Outline every leukocyte.
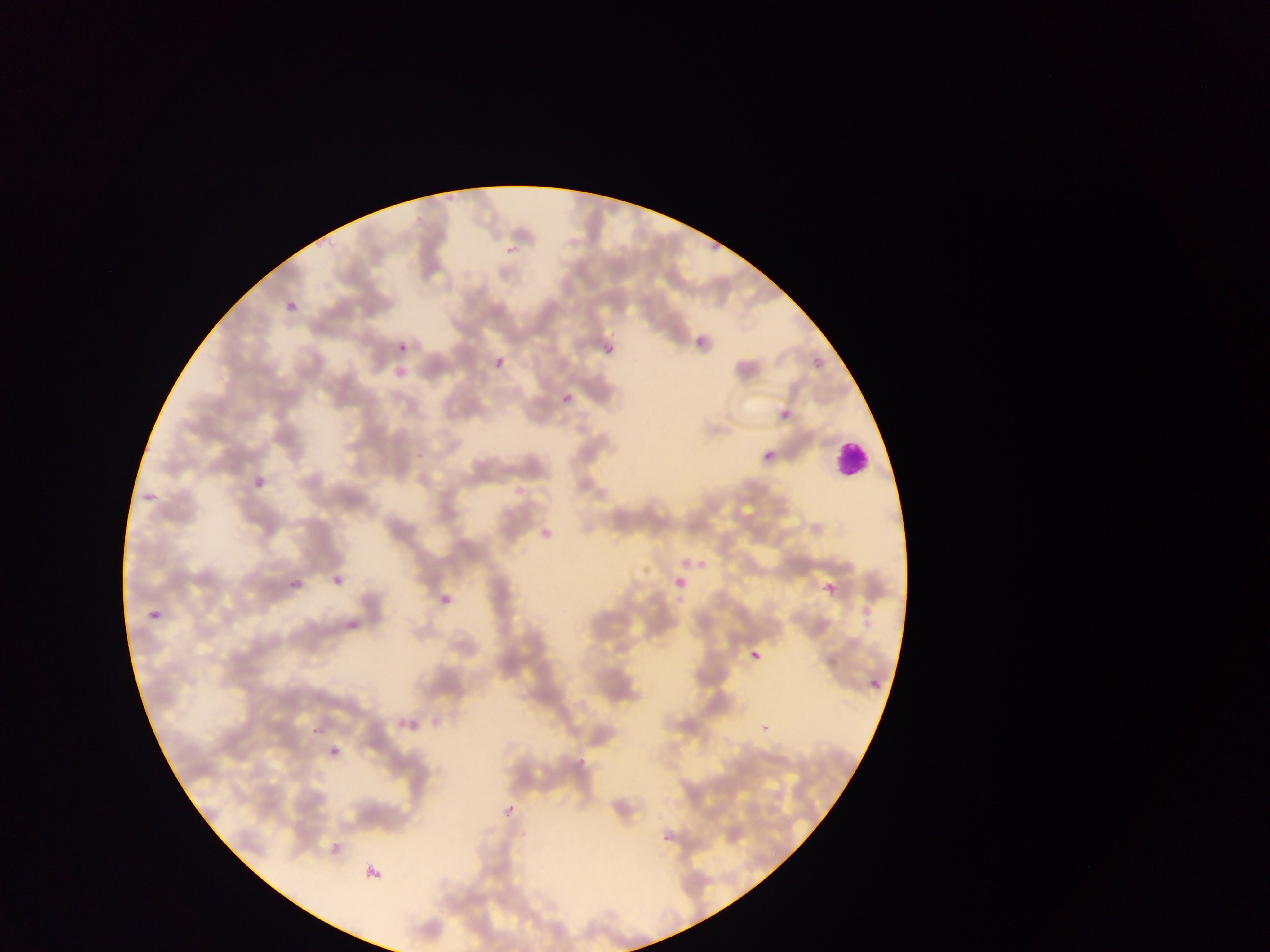

Approximate bounding boxes as (left, top, right, bottom) in pixels.
Leukocytes: (829, 441, 869, 478).

Summary:
  - Malaria parasite locations: (505, 244, 519, 255), (694, 338, 703, 346), (399, 344, 407, 351), (605, 347, 614, 354), (496, 356, 504, 366), (811, 357, 822, 367), (563, 394, 573, 403), (782, 411, 792, 420), (762, 452, 771, 458), (288, 575, 303, 589), (869, 679, 881, 690)
  - Capture: mobile-phone photograph through a microscope
  - Image size: 1270×952 pixels
  - Field of view: single
  - Preparation: thin blood film
  - Country: Ghana